Locate every blood parasite and identify its species.
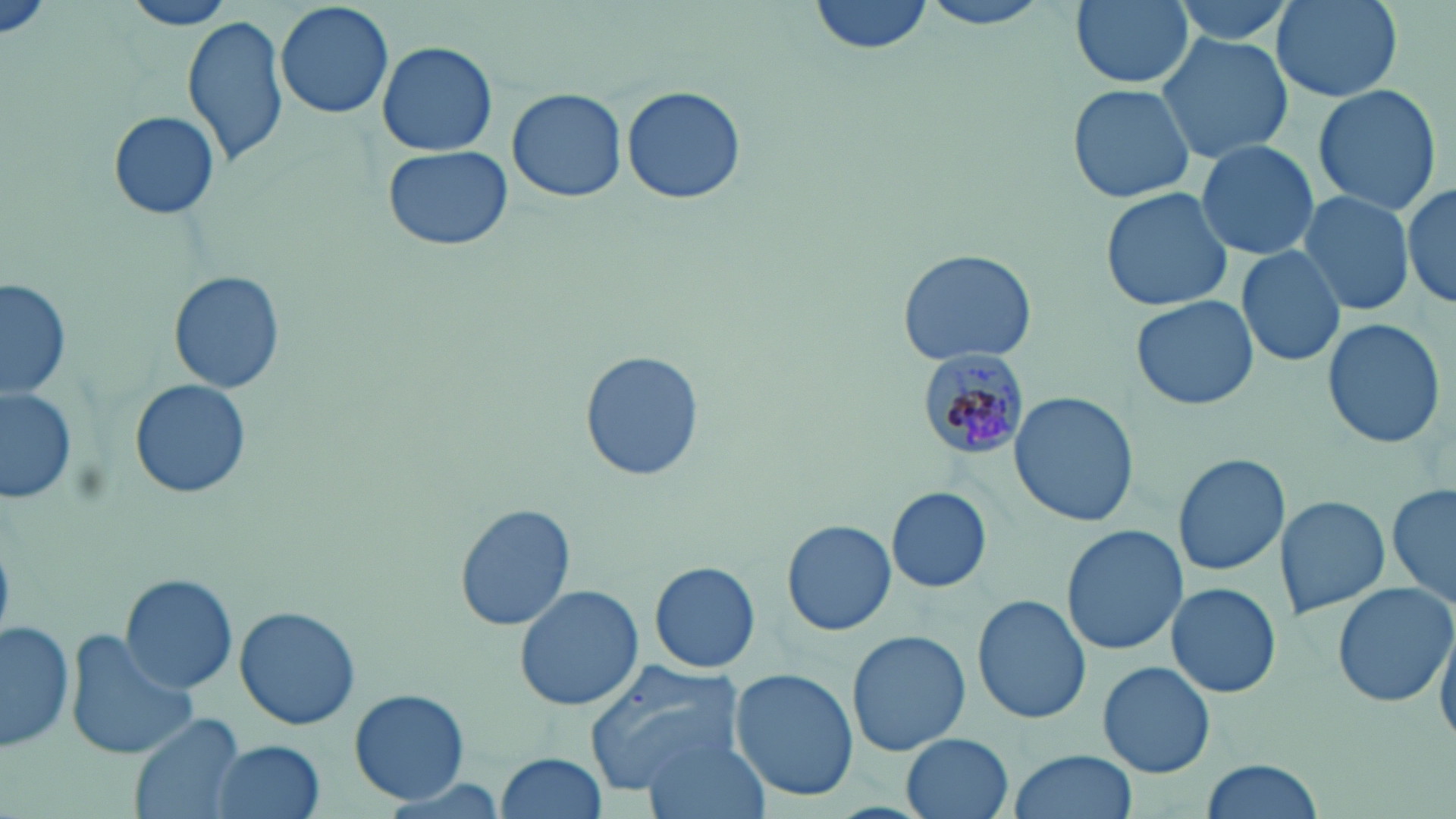
Approximate bounding boxes as [x1, y1, x2, y2] in pixels.
Plasmodium malariae-infected red blood cells: [917, 348, 1031, 460].
No Plasmodium falciparum, Plasmodium ovale, Plasmodium vivax, Babesia divergens, or Trypanosoma brucei observed.

slide_level_diagnosis: Plasmodium malariae
stain: May-Grünwald-Giemsa
field_of_view: single
image_size: 1456×819 pixels
preparation: thin blood film
modality: light microscopy
magnification: 1000x
uninfected_red_blood_cell_locations: 'approximate bounding boxes as [x1, y1, x2, y2] in pixels: [1, 0, 54, 43], [118, 0, 241, 31], [810, 0, 934, 57], [912, 0, 1061, 30], [1067, 0, 1196, 91], [1164, 0, 1300, 49], [1270, 0, 1404, 103], [276, 1, 395, 120], [181, 14, 288, 167], [1156, 31, 1293, 165], [377, 40, 497, 156], [1067, 82, 1197, 205], [1311, 84, 1442, 214], [621, 86, 747, 205], [506, 88, 629, 202], [108, 109, 221, 220], [1194, 139, 1320, 261], [382, 145, 513, 253], [1400, 182, 1455, 310], [1099, 188, 1235, 313], [1297, 190, 1417, 317], [1236, 245, 1347, 368], [896, 248, 1039, 367], [168, 272, 284, 393], [2, 278, 71, 401], [1131, 294, 1259, 411], [1320, 316, 1448, 449], [582, 353, 702, 481], [129, 377, 253, 500], [0, 386, 79, 507], [1009, 391, 1136, 528], [1172, 453, 1288, 576], [1387, 485, 1455, 617], [886, 487, 992, 593], [1276, 496, 1390, 618], [455, 501, 575, 631], [782, 519, 897, 638], [1060, 525, 1185, 655], [648, 561, 761, 673], [119, 573, 238, 694], [1169, 581, 1282, 700], [1332, 582, 1453, 708], [514, 584, 644, 712], [971, 594, 1091, 723], [235, 607, 363, 730], [1433, 611, 1456, 751], [1, 620, 75, 753], [845, 628, 972, 758], [67, 630, 197, 760], [581, 660, 745, 794], [1099, 662, 1215, 779], [730, 669, 859, 802], [350, 690, 468, 802], [131, 712, 245, 819], [640, 731, 770, 819], [900, 733, 1013, 819], [208, 739, 324, 819], [1010, 749, 1136, 819], [497, 752, 606, 819], [1200, 759, 1324, 817]'